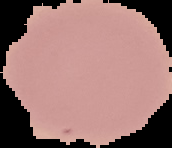
Result: no malaria parasites detected. Segmented cell region on a black background. Image is 172×148 pixels. From a thin blood film.